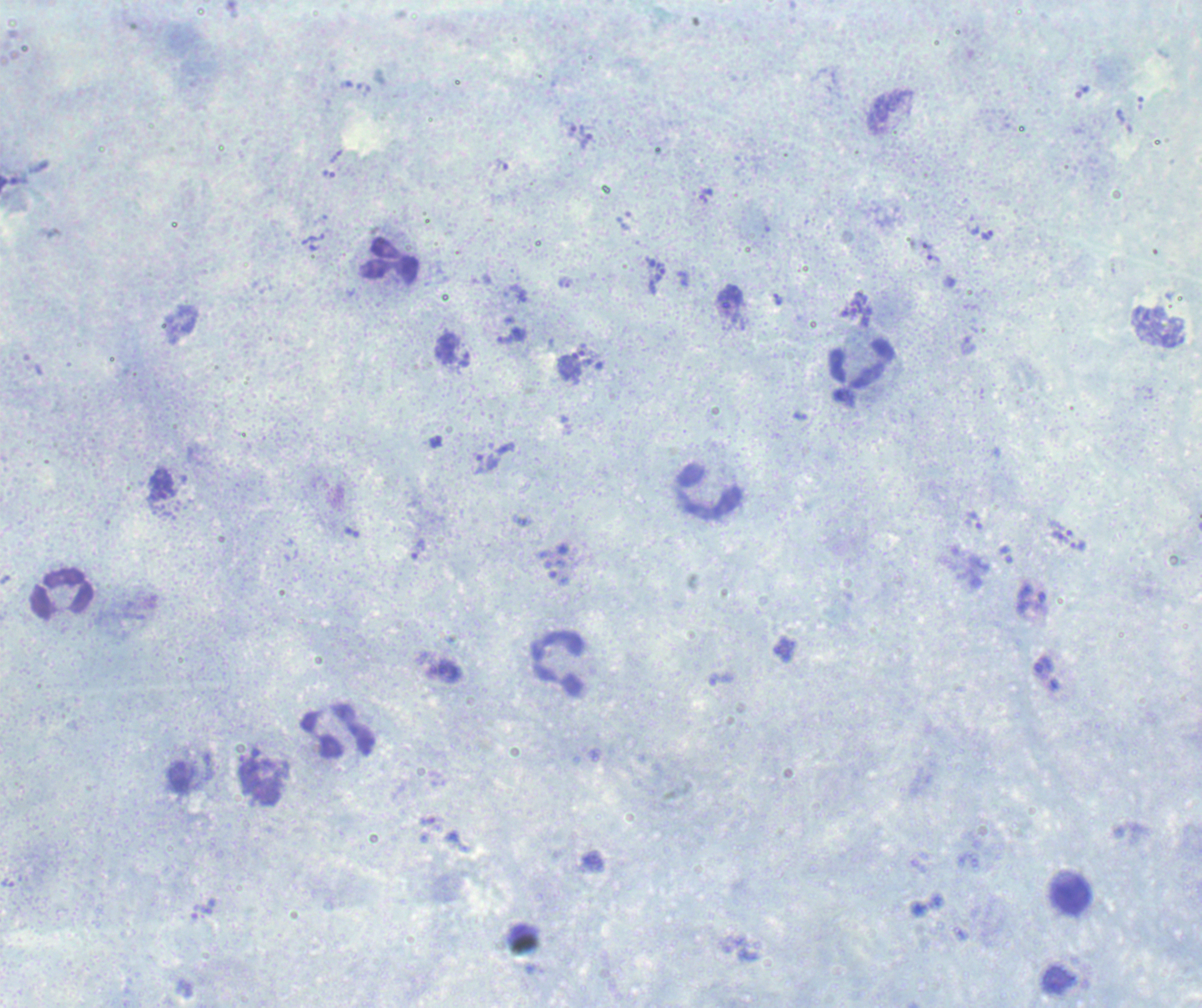 Image is 1202×1008 pixels. Romanowsky-stained preparation. Thick smear of blood. Single field of view.